Assess this cell for malaria.
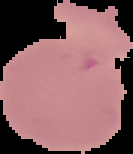

Uninfected.

Segmented cell region on a black background. From a thin blood film. Image is 133×154 pixels.